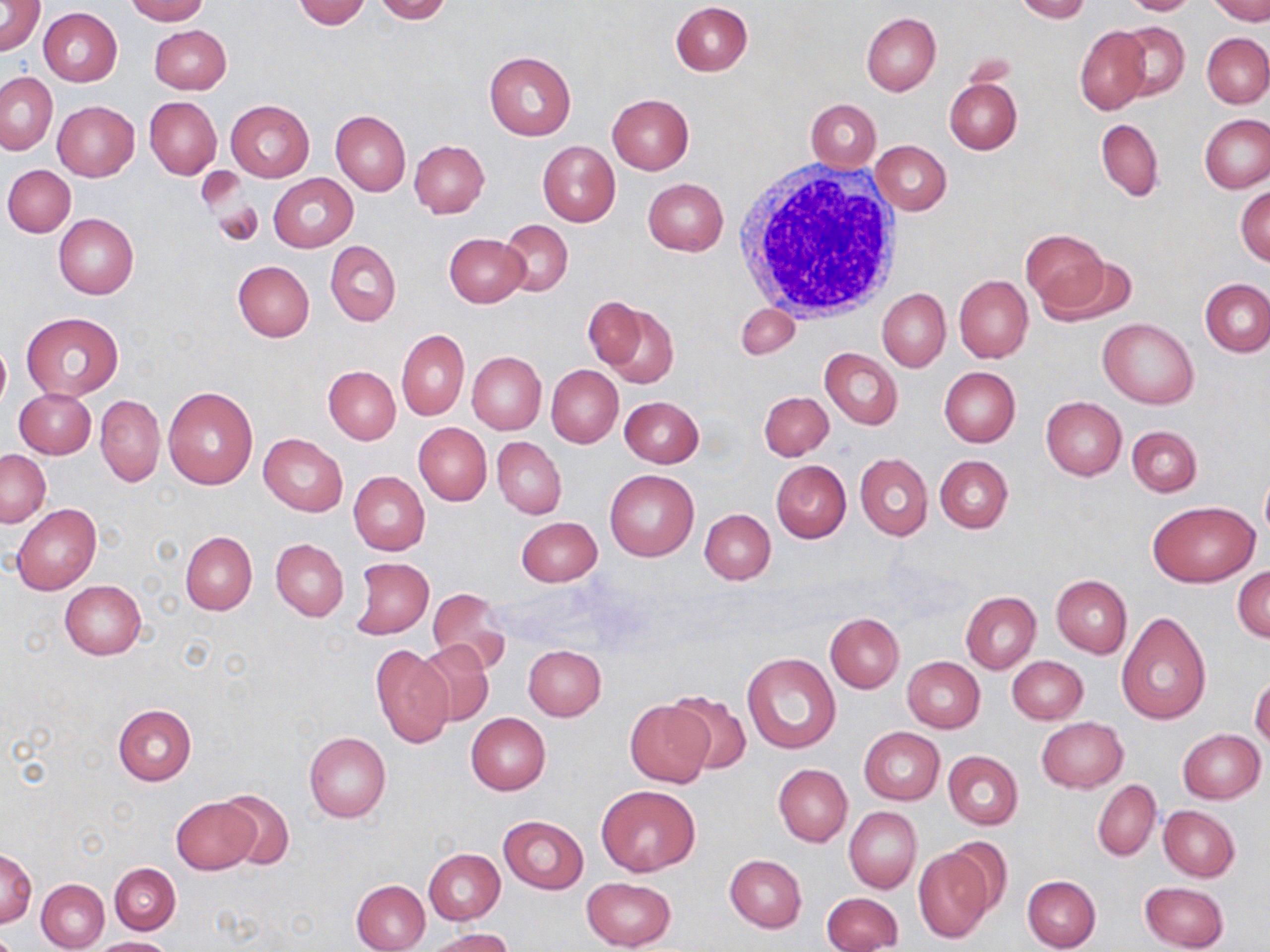
Summary:
  - Coordinate format: approximate bounding boxes as [x1, y1, x2, y2] in pixels
  - Uninfected red blood cell locations: [123, 0, 208, 24], [292, 0, 370, 29], [374, 0, 452, 24], [1014, 0, 1089, 23], [1121, 0, 1204, 15], [1210, 0, 1270, 24], [0, 1, 45, 56], [671, 2, 752, 76], [39, 7, 122, 87], [861, 12, 940, 95], [1114, 22, 1190, 101], [149, 25, 231, 94], [1075, 26, 1150, 114], [1201, 33, 1270, 108], [483, 51, 575, 141], [1, 72, 57, 154], [944, 79, 1021, 154], [607, 93, 694, 174], [145, 97, 222, 179], [806, 99, 881, 171], [226, 100, 315, 181], [53, 101, 138, 181], [330, 111, 411, 195], [1199, 113, 1269, 193], [1096, 119, 1164, 200], [409, 140, 489, 218], [537, 140, 621, 227], [870, 141, 951, 215], [3, 165, 75, 237], [197, 168, 244, 213], [268, 174, 358, 252], [642, 178, 728, 255], [1235, 185, 1270, 267], [208, 192, 263, 246], [54, 213, 138, 300], [498, 220, 574, 296], [1022, 227, 1113, 316], [445, 234, 529, 308], [325, 241, 401, 326], [1040, 254, 1139, 327], [234, 261, 316, 342], [954, 276, 1033, 364], [1201, 278, 1269, 356], [877, 288, 951, 372], [583, 296, 647, 369], [591, 301, 679, 388], [735, 302, 800, 358], [21, 311, 124, 401], [1098, 318, 1198, 409], [397, 330, 470, 420], [0, 338, 9, 413], [821, 348, 903, 429], [467, 352, 546, 435], [545, 365, 622, 448], [324, 366, 400, 444], [939, 367, 1020, 447], [164, 387, 257, 490], [14, 389, 97, 458], [759, 391, 833, 461], [619, 395, 704, 468], [96, 396, 165, 485], [1041, 397, 1126, 480], [414, 423, 491, 506], [1127, 425, 1202, 498], [259, 434, 347, 516], [493, 437, 566, 519], [1, 450, 50, 526], [856, 454, 932, 540], [935, 456, 1013, 533], [772, 460, 851, 543], [604, 469, 699, 562], [348, 471, 430, 555], [1260, 472, 1270, 543], [1148, 500, 1259, 586], [12, 503, 101, 596], [699, 507, 775, 584], [517, 517, 602, 586], [180, 532, 256, 615], [271, 538, 349, 621], [351, 557, 433, 639], [1232, 566, 1270, 642], [1051, 575, 1132, 657], [60, 581, 146, 660], [427, 588, 511, 676], [961, 592, 1041, 673], [1117, 610, 1211, 726], [826, 612, 904, 693], [414, 639, 494, 728], [523, 645, 606, 721], [371, 647, 453, 748], [742, 652, 840, 754], [1007, 655, 1089, 725], [902, 656, 984, 732], [1250, 677, 1270, 750], [665, 690, 753, 775], [626, 700, 712, 787], [113, 703, 196, 786], [465, 713, 551, 794], [1036, 717, 1128, 793], [859, 727, 944, 804], [1177, 729, 1265, 803], [304, 731, 391, 821], [942, 750, 1023, 830], [774, 764, 852, 846], [1092, 780, 1161, 860], [598, 784, 699, 875], [218, 788, 295, 869], [171, 797, 257, 874], [1158, 805, 1240, 882], [844, 806, 921, 893], [1150, 807, 1232, 952], [498, 815, 588, 893], [912, 844, 995, 942], [423, 848, 504, 923], [1, 850, 36, 927], [725, 854, 806, 933], [109, 862, 180, 934], [1021, 875, 1100, 951], [581, 876, 678, 950], [37, 878, 109, 951], [352, 879, 429, 951], [1139, 881, 1229, 951], [821, 893, 904, 952], [429, 928, 514, 952], [96, 937, 173, 952]
  - White blood cell locations: [732, 158, 907, 327]
  - Slide-level diagnosis: no evidence of blood parasites
  - Image size: 1270×952 pixels
  - Preparation: thin blood film
  - Modality: optical microscopy
  - Magnification: 1000x
  - Field of view: single
  - Stain: May-Grünwald-Giemsa